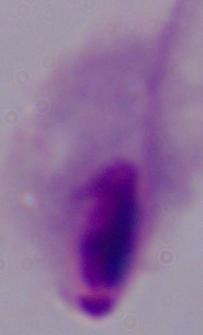
identification: trichomonad
modality: photomicrograph
magnification: 1000x